Classify this cell by malaria status.
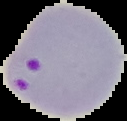

It is parasitized.

From a thin blood smear. Segmented cell region on a black background. Image is 127×121 pixels.